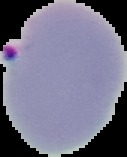
Summary:
  - Result: malaria parasites identified
  - Preparation: thin blood smear
  - Image type: segmented cell region with the area outside set to black
  - Image size: 127×157 pixels